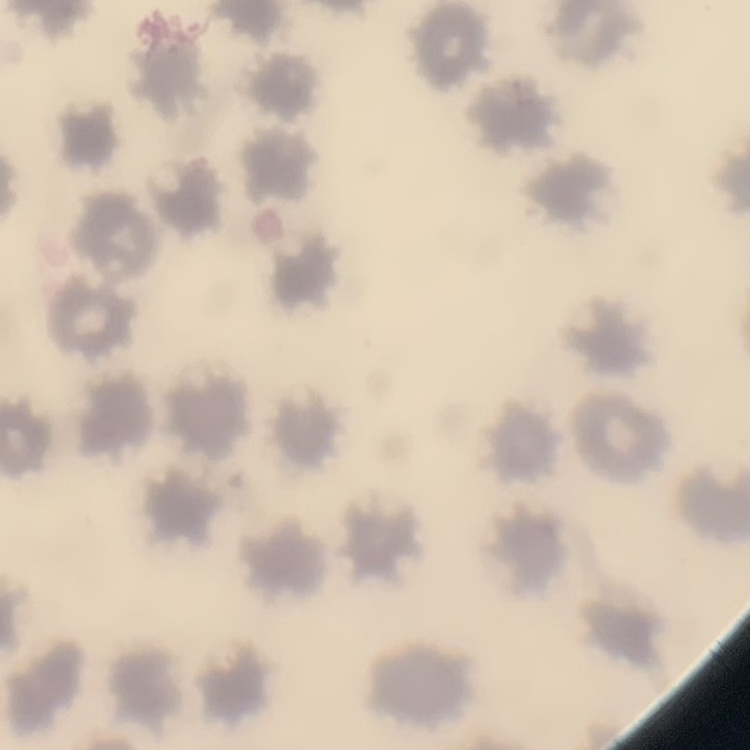
Summary:
  - Erythrocyte morphology: no rouleaux formation
  - Image type: square crop of a larger photomicrograph
  - Stain: Field's or Giemsa
  - Preparation: thin blood film